Comment on the morphology of the erythrocytes.
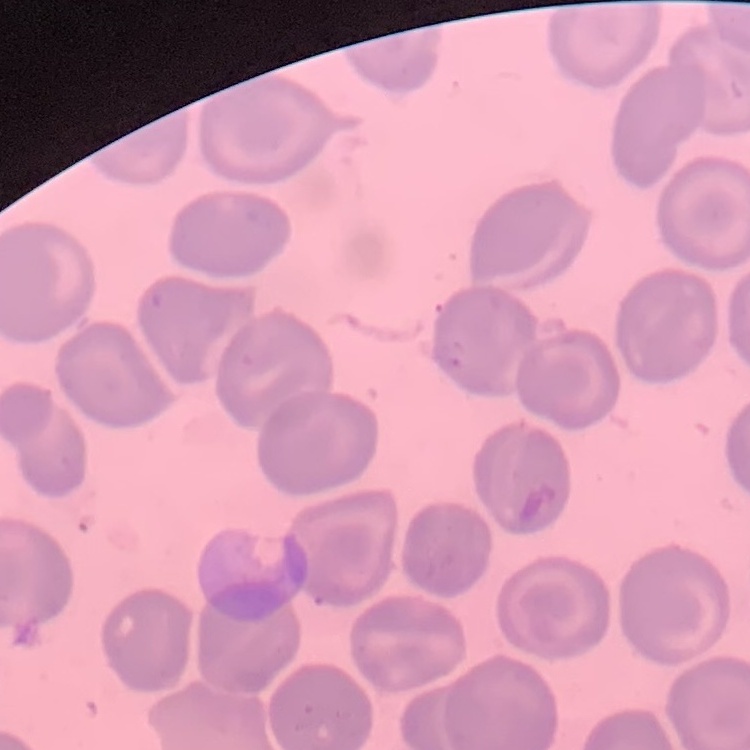

No rouleaux formation.

Summary:
  - Stain: Field's or Giemsa
  - Image type: one tile cut from a larger photomicrograph
  - Preparation: thin blood film